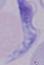
Summary:
  - Identification: trypanosome
  - Modality: micrograph
  - Magnification: 1000x